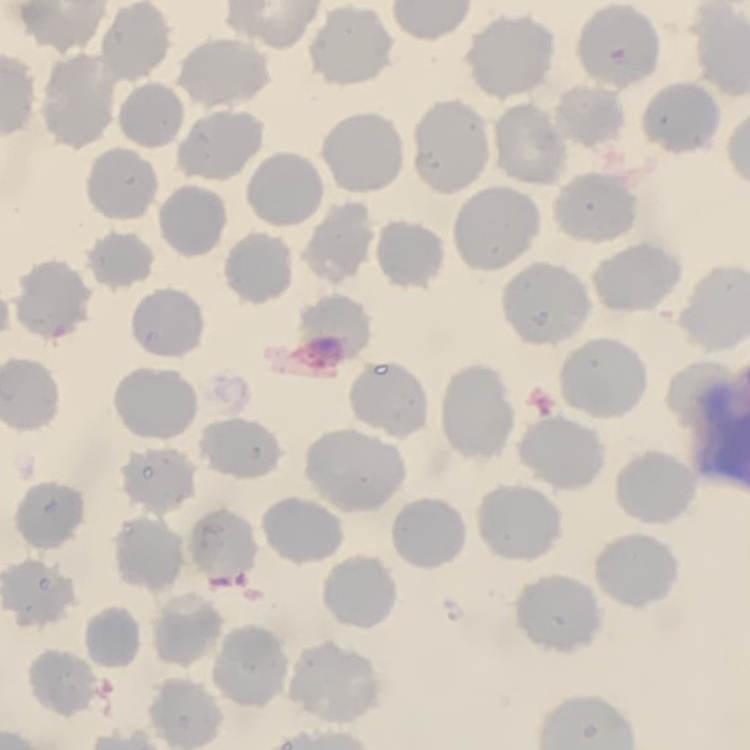
The red blood cells exhibit no rouleaux formation. Field's or Giemsa stain. Square crop of a larger photomicrograph. Thin peripheral smear.